Locate every Plasmodium parasite.
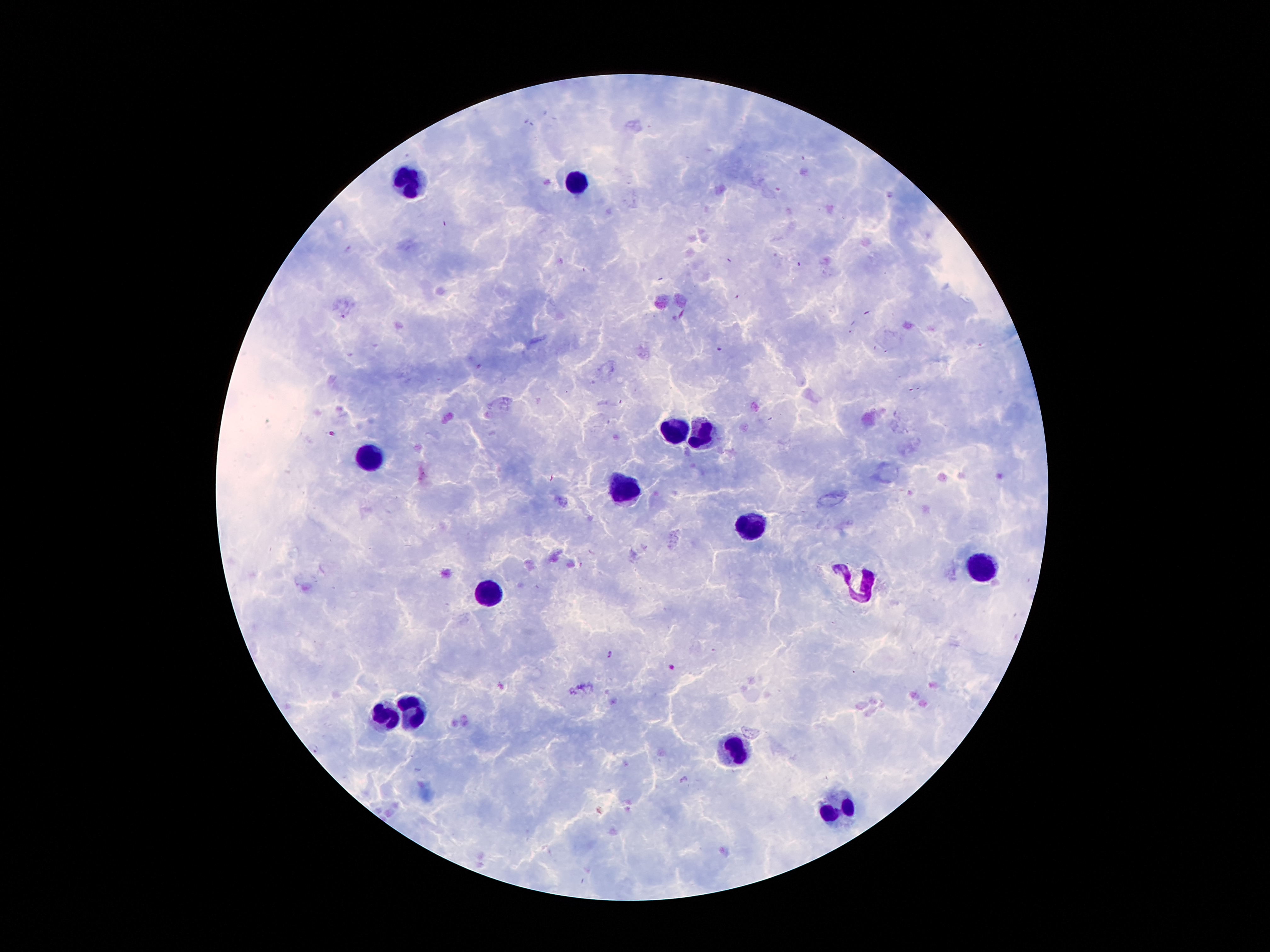
Approximate centers as [x, y] in pixels.
Plasmodium parasites: [719, 349], [331, 433], [610, 655], [672, 667], [314, 748].

{
  "patient_malaria_status": "infected with Plasmodium falciparum",
  "magnification": "100x",
  "preparation": "thick peripheral-blood smear",
  "stain": "Giemsa",
  "field_of_view": "single",
  "image_size": "1270×952 pixels",
  "leukocyte_locations": "approximate centers as [x, y] in pixels: [574, 179], [415, 182], [667, 431], [708, 434], [372, 452], [624, 490], [753, 531], [980, 565], [860, 590], [487, 592], [383, 715], [415, 715], [728, 749], [837, 813]",
  "capture": "smartphone camera through the microscope eyepiece"
}